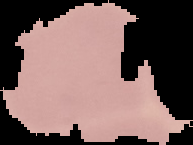
From a thin blood film. Malaria status: uninfected. Cell region segmented out of the field of view; the surrounding area is masked to black. Image is 193×145 pixels.